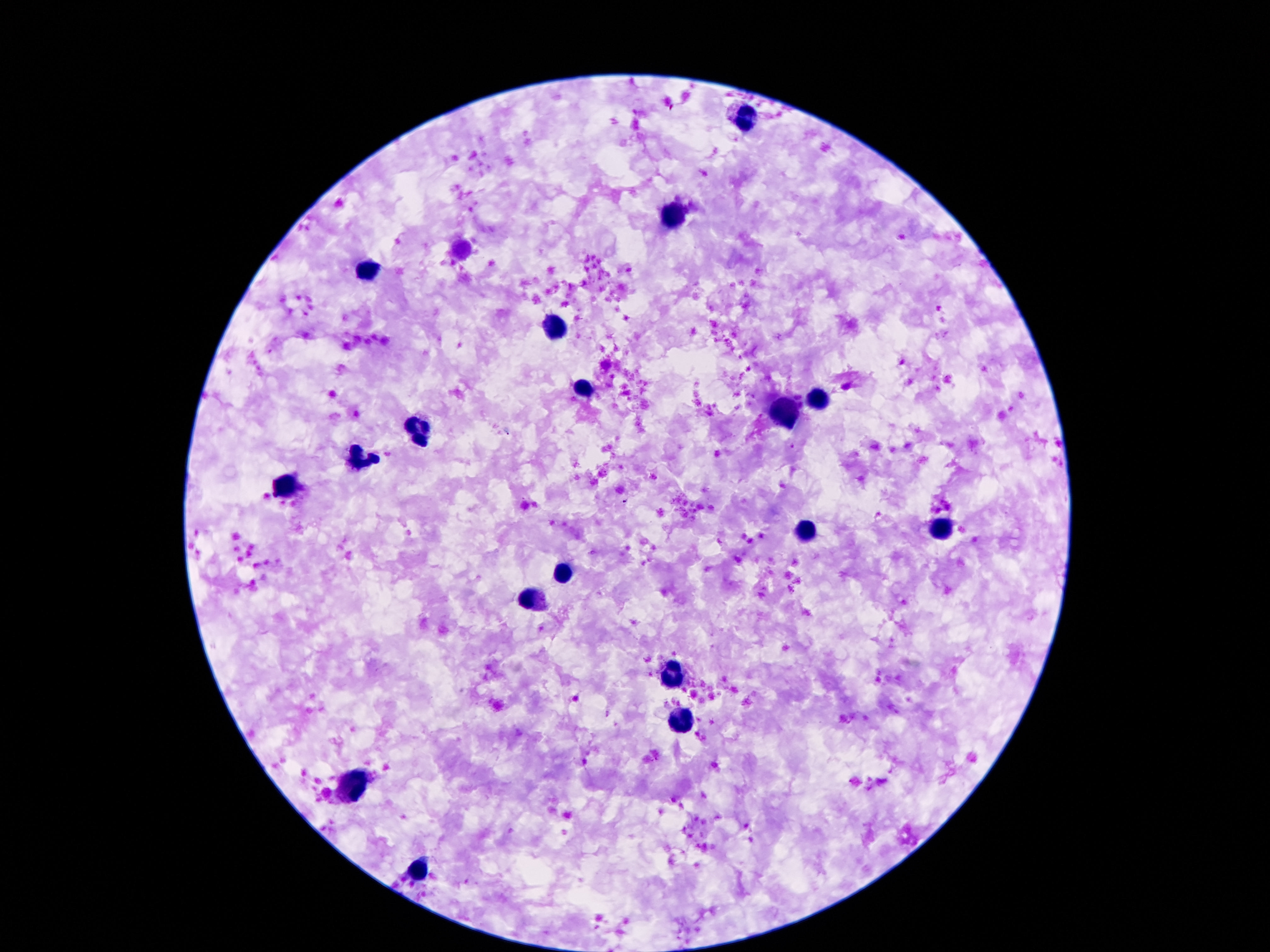
field of view = single
patient malaria status = not infected
stain = Giemsa
image size = 1270×952 pixels
capture = smartphone camera through the microscope eyepiece
leukocyte locations = approximate centers as {x, y} in pixels: {745, 119}, {674, 214}, {369, 269}, {555, 328}, {584, 389}, {819, 399}, {783, 415}, {420, 431}, {360, 458}, {289, 488}, {940, 530}, {803, 533}, {564, 573}, {533, 600}, {674, 676}, {677, 721}, {355, 786}, {420, 870}
preparation = thick blood smear
magnification = 100x